Identify the preparation type.
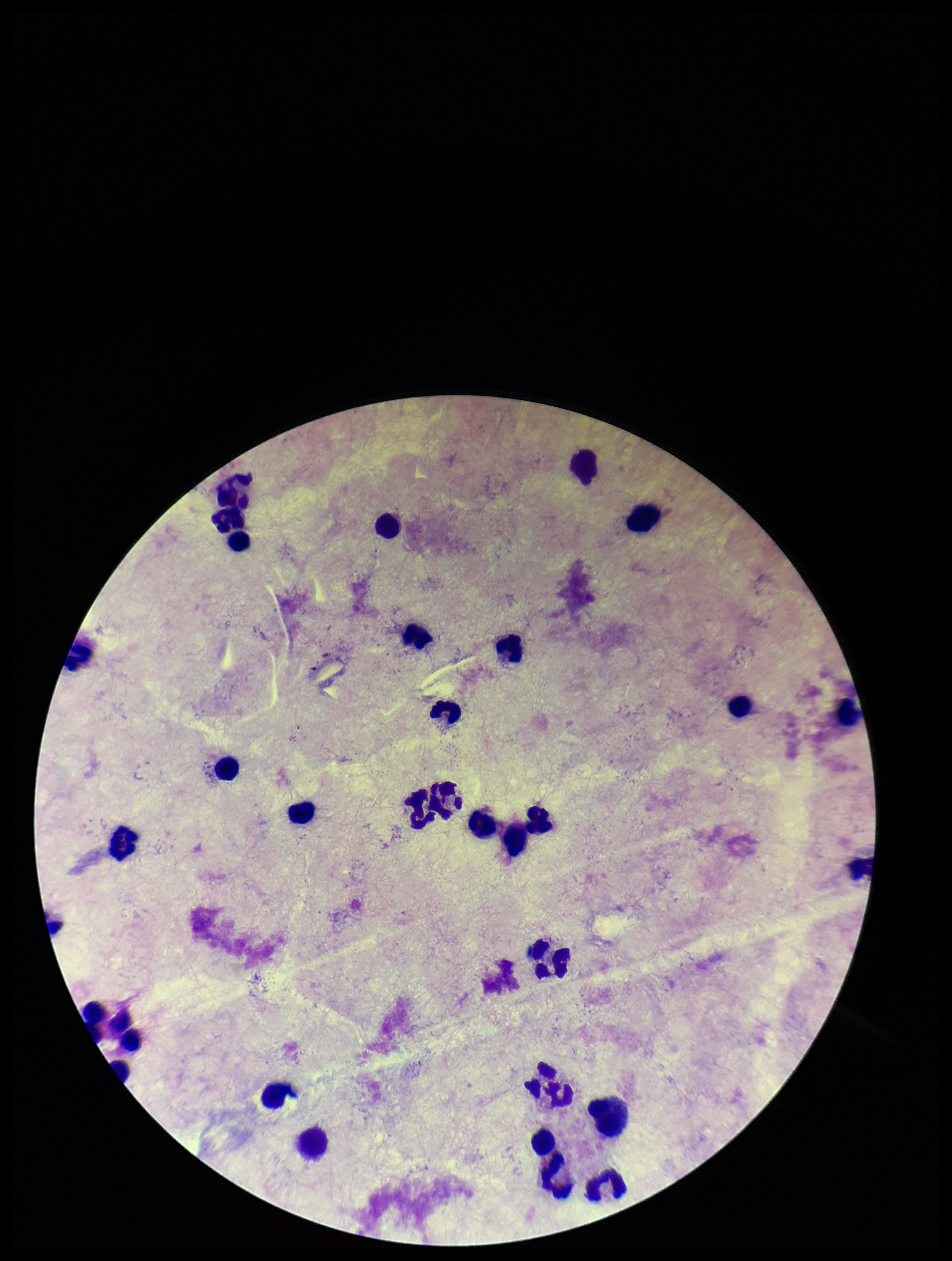

A thick smear.

Smartphone photograph taken through the eyepiece of a microscope. Plasmodium parasites: none identified. Stained with Giemsa. Patient malaria status: negative. Single field of view. Image is 952×1261 pixels. Leukocyte count: 33. Parasite count: 0.